State the blood parasite species.
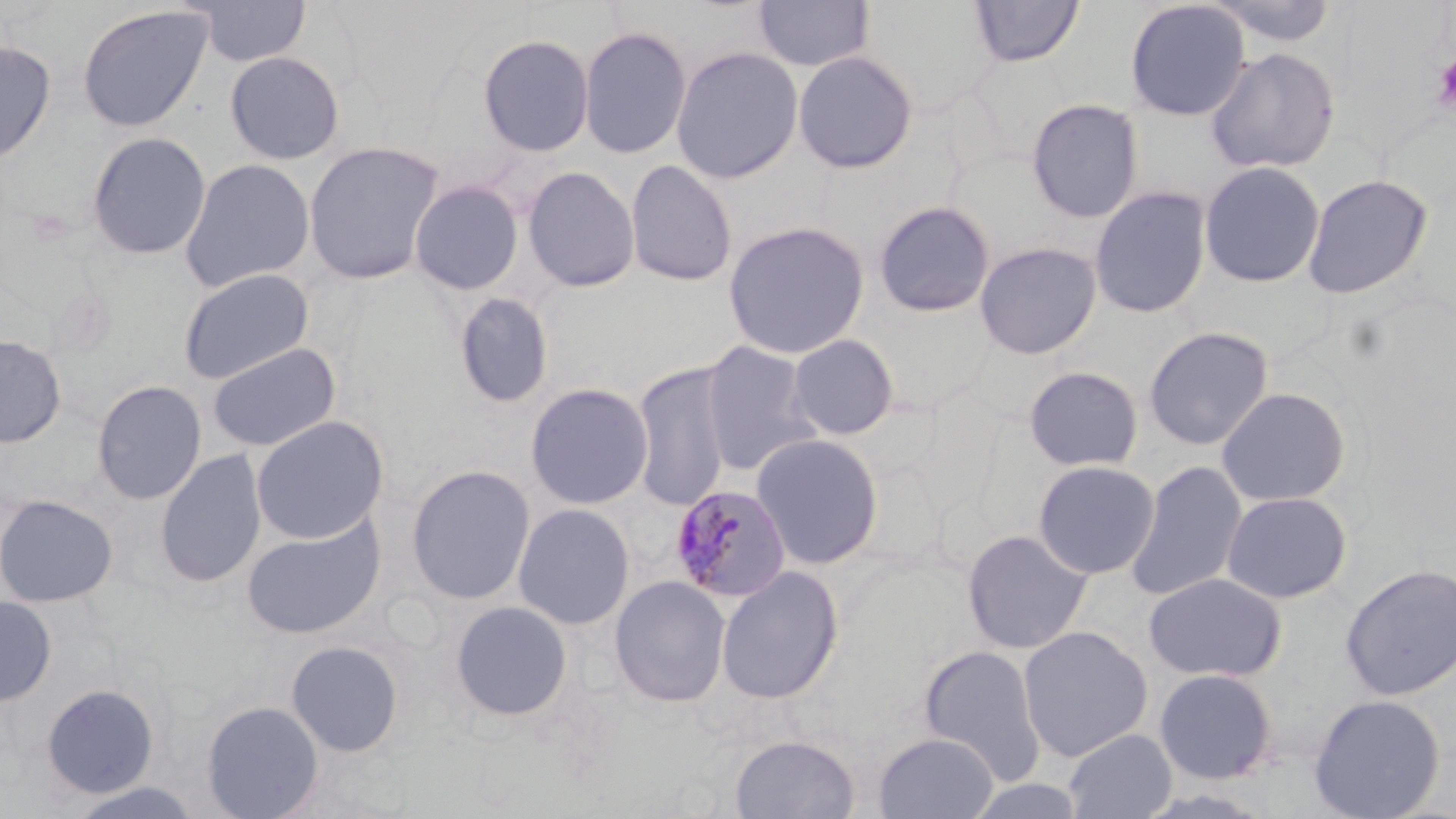
Plasmodium malariae.

Approximate bounding boxes as (x1, y1, x2, y2) in pixels. Platelet locations: (1432, 54, 1456, 112). Plasmodium malariae-infected red blood cell locations: (669, 484, 793, 603). Uninfected red blood cell locations: (187, 0, 312, 67), (753, 0, 874, 71), (968, 0, 1085, 68), (1206, 0, 1340, 47), (1124, 1, 1251, 121), (76, 5, 213, 132), (578, 25, 692, 159), (477, 33, 595, 157), (0, 40, 56, 164), (671, 46, 804, 183), (1205, 46, 1341, 173), (793, 50, 919, 174), (225, 51, 345, 165), (1026, 97, 1144, 223), (86, 132, 211, 259), (304, 140, 445, 285), (179, 158, 316, 292), (625, 160, 738, 287), (1198, 161, 1325, 288), (522, 165, 640, 293), (1302, 173, 1434, 299), (409, 179, 524, 295), (1088, 186, 1212, 318), (873, 200, 996, 317), (723, 220, 870, 359), (974, 241, 1102, 359), (178, 268, 314, 384), (453, 292, 554, 409), (1143, 326, 1274, 450), (0, 334, 66, 447), (787, 334, 899, 440), (699, 341, 820, 476), (207, 342, 341, 452), (631, 361, 734, 512), (1023, 365, 1145, 471), (92, 379, 207, 505), (525, 382, 653, 510), (1216, 386, 1351, 507), (251, 415, 389, 544), (751, 433, 885, 569), (155, 449, 266, 588), (1125, 459, 1249, 601), (1032, 460, 1160, 579), (405, 465, 536, 604), (1221, 491, 1352, 603), (0, 493, 118, 607), (512, 503, 635, 630), (241, 516, 386, 639), (961, 529, 1093, 654), (1340, 563, 1456, 701), (715, 565, 844, 705), (1144, 571, 1287, 681), (609, 575, 731, 707), (0, 595, 57, 706), (450, 600, 573, 722), (1018, 625, 1153, 762), (286, 640, 405, 757), (918, 644, 1048, 784), (1154, 667, 1279, 784), (41, 684, 159, 798), (1308, 693, 1446, 819), (201, 700, 324, 819), (1062, 729, 1177, 819), (873, 732, 999, 818), (729, 734, 861, 819), (62, 780, 206, 819). Thin blood film. Single field of view. May-Grünwald-Giemsa-stained preparation. Image is 1456×819 pixels. Light microscopy. 1000x magnification.